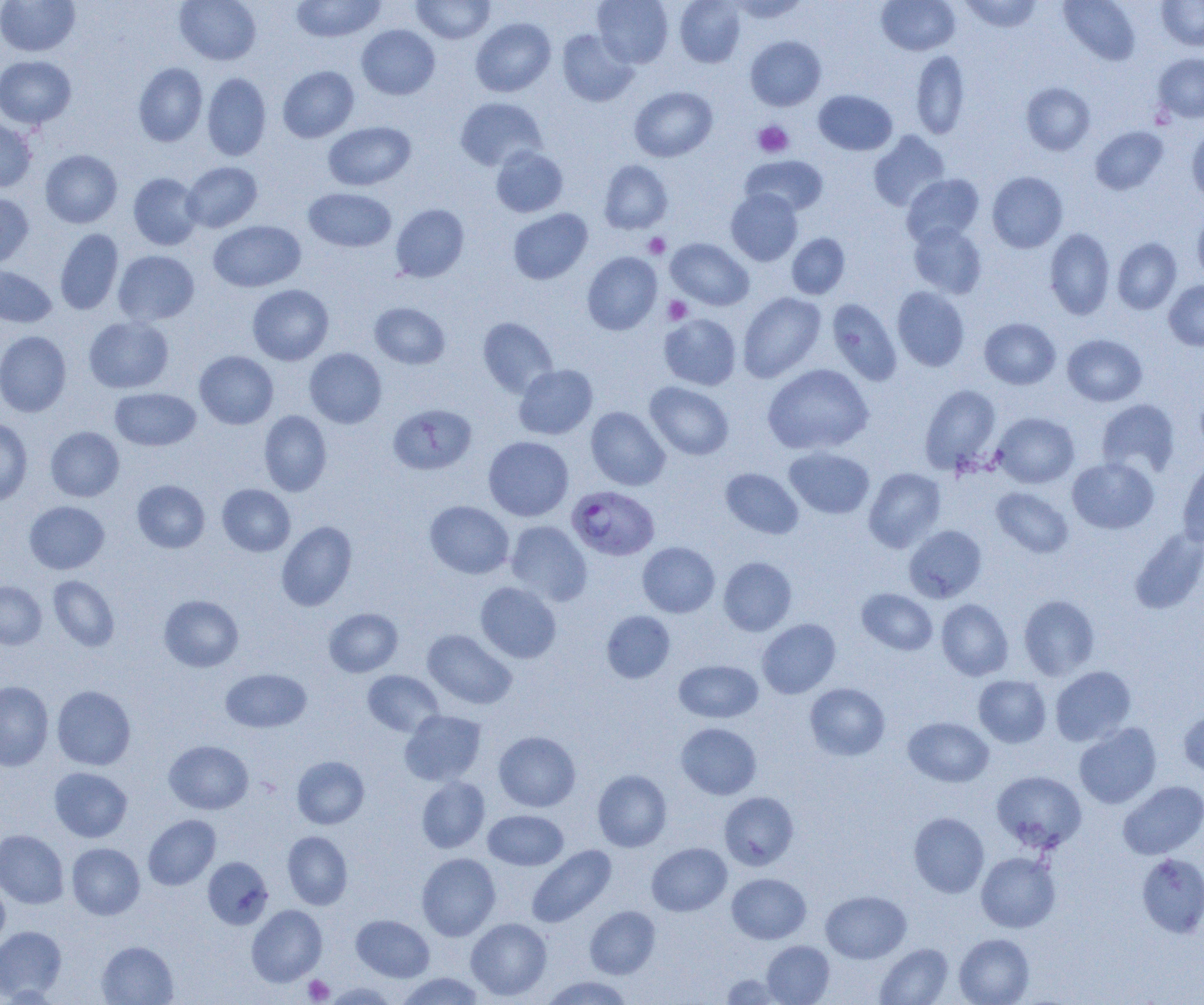 Approximate bounding boxes as (x1, y1, x2, y2) in pixels. Platelet locations: (753, 121, 794, 158), (643, 233, 670, 258), (663, 296, 692, 324), (303, 975, 334, 1003). Uninfected red blood cell locations: (0, 0, 80, 56), (175, 0, 261, 65), (290, 0, 386, 42), (411, 0, 495, 44), (592, 0, 673, 67), (674, 0, 745, 67), (726, 0, 811, 23), (877, 0, 960, 55), (959, 0, 1043, 33), (1059, 0, 1140, 65), (1157, 0, 1204, 50), (470, 18, 556, 97), (356, 24, 440, 100), (557, 29, 638, 107), (745, 36, 826, 111), (910, 50, 970, 139), (1153, 53, 1204, 122), (0, 56, 77, 129), (133, 62, 208, 146), (278, 66, 359, 142), (202, 73, 271, 161), (1021, 82, 1095, 155), (629, 86, 717, 162), (814, 90, 897, 155), (455, 97, 547, 171), (0, 118, 37, 192), (323, 121, 415, 191), (1090, 126, 1168, 195), (1186, 129, 1204, 206), (868, 131, 950, 211), (490, 147, 568, 217), (40, 149, 122, 228), (740, 155, 828, 216), (598, 160, 673, 234), (183, 162, 262, 232), (986, 171, 1068, 253), (128, 173, 203, 250), (901, 174, 984, 246), (303, 188, 397, 252), (726, 189, 803, 266), (0, 193, 34, 268), (391, 204, 469, 282), (508, 208, 592, 285), (1192, 212, 1204, 284), (208, 220, 306, 292), (909, 222, 987, 299), (1044, 228, 1115, 319), (55, 229, 123, 315), (787, 233, 850, 299), (665, 238, 754, 311), (1112, 238, 1182, 314), (113, 250, 199, 325), (582, 252, 662, 335), (0, 265, 57, 328), (1164, 280, 1204, 351), (248, 285, 334, 365), (892, 286, 970, 371), (738, 292, 825, 382), (826, 298, 902, 386), (370, 302, 450, 369), (659, 313, 741, 390), (84, 316, 174, 393), (478, 317, 558, 398), (979, 318, 1060, 389), (0, 331, 71, 417), (1062, 334, 1147, 406), (304, 348, 387, 428), (194, 350, 278, 429), (762, 363, 873, 455), (514, 364, 598, 439), (645, 381, 734, 460), (920, 385, 1001, 474), (110, 388, 201, 451), (1096, 399, 1180, 478), (388, 404, 476, 475), (586, 406, 670, 490), (259, 410, 332, 496), (991, 412, 1079, 488), (0, 418, 33, 506), (46, 426, 124, 501), (483, 436, 574, 521), (784, 447, 875, 519), (1067, 456, 1159, 534), (1177, 457, 1204, 547), (863, 467, 946, 553), (720, 468, 803, 539), (132, 480, 210, 553), (217, 484, 295, 556), (991, 487, 1074, 558), (24, 500, 109, 574), (425, 501, 514, 579), (276, 521, 357, 611), (506, 521, 591, 606), (904, 525, 987, 603), (1130, 527, 1204, 614), (637, 542, 720, 617), (718, 557, 797, 636), (48, 575, 120, 652), (0, 581, 47, 649), (476, 582, 561, 663), (857, 588, 937, 655), (159, 595, 243, 672), (1018, 595, 1100, 680), (936, 599, 1013, 681), (324, 608, 403, 677), (601, 610, 675, 683), (757, 619, 840, 698), (422, 629, 517, 709), (674, 660, 763, 723), (1050, 665, 1136, 746), (221, 668, 311, 733), (363, 670, 443, 737), (973, 675, 1051, 747), (0, 680, 53, 771), (805, 682, 890, 761), (52, 685, 136, 770), (1178, 707, 1204, 779), (400, 710, 486, 785), (903, 716, 993, 787), (676, 722, 762, 799), (1073, 722, 1162, 809), (494, 731, 581, 811), (164, 740, 253, 814), (292, 756, 369, 829), (49, 767, 132, 842), (593, 770, 672, 852), (991, 770, 1087, 853), (416, 776, 490, 853), (1118, 780, 1204, 859), (719, 791, 799, 870), (483, 809, 568, 870), (909, 812, 989, 897), (143, 815, 220, 890), (0, 830, 68, 908), (282, 831, 353, 909), (67, 843, 145, 919), (647, 843, 732, 916), (527, 845, 616, 927), (976, 851, 1060, 932), (417, 853, 501, 941), (1136, 853, 1204, 938), (203, 857, 273, 929), (727, 873, 811, 944), (0, 879, 10, 951), (820, 890, 911, 963), (247, 905, 327, 986), (585, 906, 660, 978), (351, 915, 434, 982), (466, 918, 551, 1000), (0, 925, 67, 1002), (954, 933, 1034, 1005), (96, 941, 178, 1005), (762, 941, 834, 1004), (875, 943, 954, 1005), (395, 972, 487, 1004), (719, 973, 790, 1004), (540, 975, 634, 1004), (321, 982, 400, 1004). Plasmodium falciparum-infected red blood cell locations: (567, 485, 660, 561). Slide-level diagnosis: Plasmodium falciparum. Light microscopy. Image is 1204×1005 pixels. Thin blood film. Single field of view. 1000x magnification.